Outline each Plasmodium ovale-infected red blood cell.
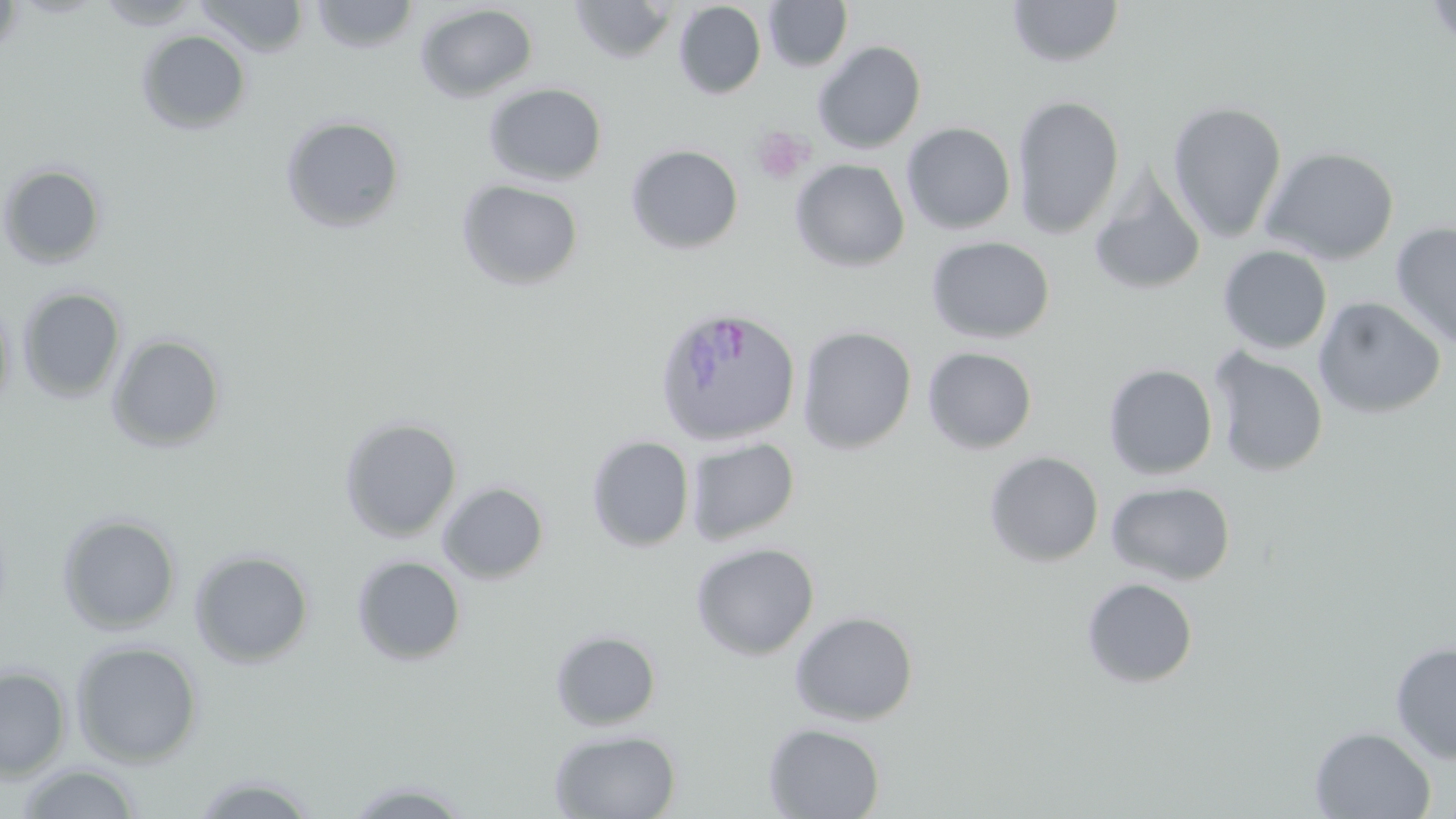
Approximate bounding boxes as (x1,y1)-(x2,y2) corner pairs in pixels.
Plasmodium ovale-infected red blood cells: (654,306)-(800,448).

Summary:
  - Uninfected red blood cell locations: (0,0)-(23,59), (95,0)-(203,29), (196,0)-(309,58), (309,0)-(421,54), (763,0)-(853,72), (1007,0)-(1125,69), (1423,0)-(1456,47), (567,1)-(679,64), (673,2)-(766,99), (415,3)-(538,103), (136,30)-(252,135), (812,40)-(927,154), (484,82)-(607,186), (1011,94)-(1125,240), (1167,100)-(1287,241), (280,114)-(406,233), (901,122)-(1016,234), (625,144)-(744,254), (1259,146)-(1400,265), (790,159)-(910,272), (0,163)-(106,269), (1089,169)-(1206,296), (456,179)-(585,291), (1390,222)-(1456,348), (925,236)-(1055,344), (1217,245)-(1333,355), (17,287)-(126,403), (0,294)-(15,418), (1312,296)-(1447,419), (797,325)-(917,454), (107,333)-(226,452), (922,346)-(1038,455), (1209,349)-(1328,478), (1103,364)-(1218,480), (339,416)-(462,542), (587,435)-(695,552), (685,435)-(800,546), (984,451)-(1104,567), (1106,480)-(1236,586), (437,481)-(550,584), (56,513)-(182,634), (690,542)-(820,661), (189,549)-(315,667), (351,555)-(467,666), (1081,577)-(1198,688), (789,611)-(919,726), (551,629)-(661,731), (70,640)-(204,766), (1390,642)-(1456,764), (0,665)-(71,781), (763,722)-(885,818), (1310,726)-(1436,818), (549,728)-(682,819), (15,763)-(143,818), (188,772)-(322,818), (341,779)-(477,817)
  - Platelet locations: (750,125)-(815,185)
  - Slide-level diagnosis: Plasmodium ovale
  - Modality: light microscopy
  - Magnification: 1000x
  - Field of view: single
  - Stain: May-Grünwald-Giemsa
  - Image size: 1456×819 pixels
  - Preparation: thin blood film